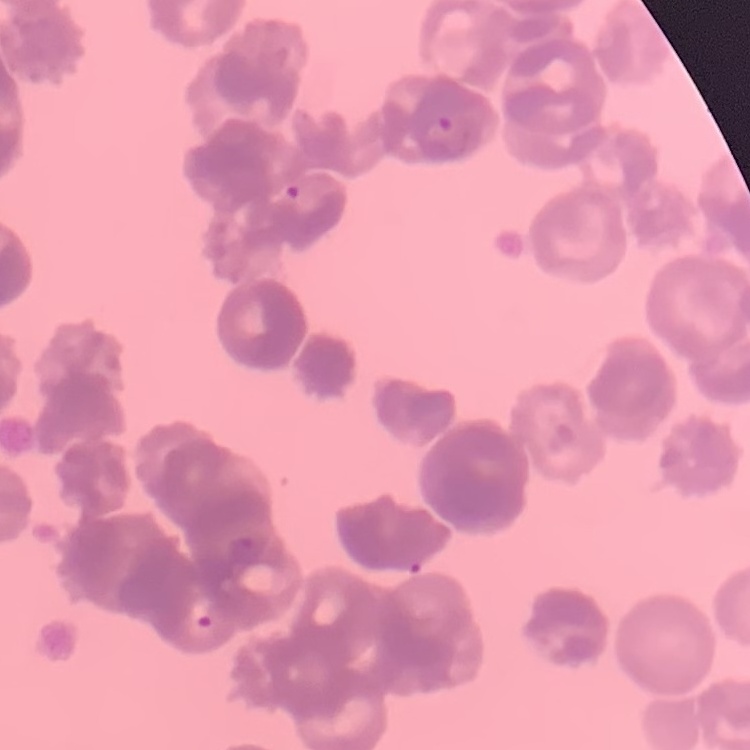

{
  "erythrocyte_morphology": "rouleaux formation",
  "stain": "Field's or Giemsa",
  "image_type": "square crop of a larger photomicrograph",
  "preparation": "thin peripheral smear"
}